State the blood parasite species.
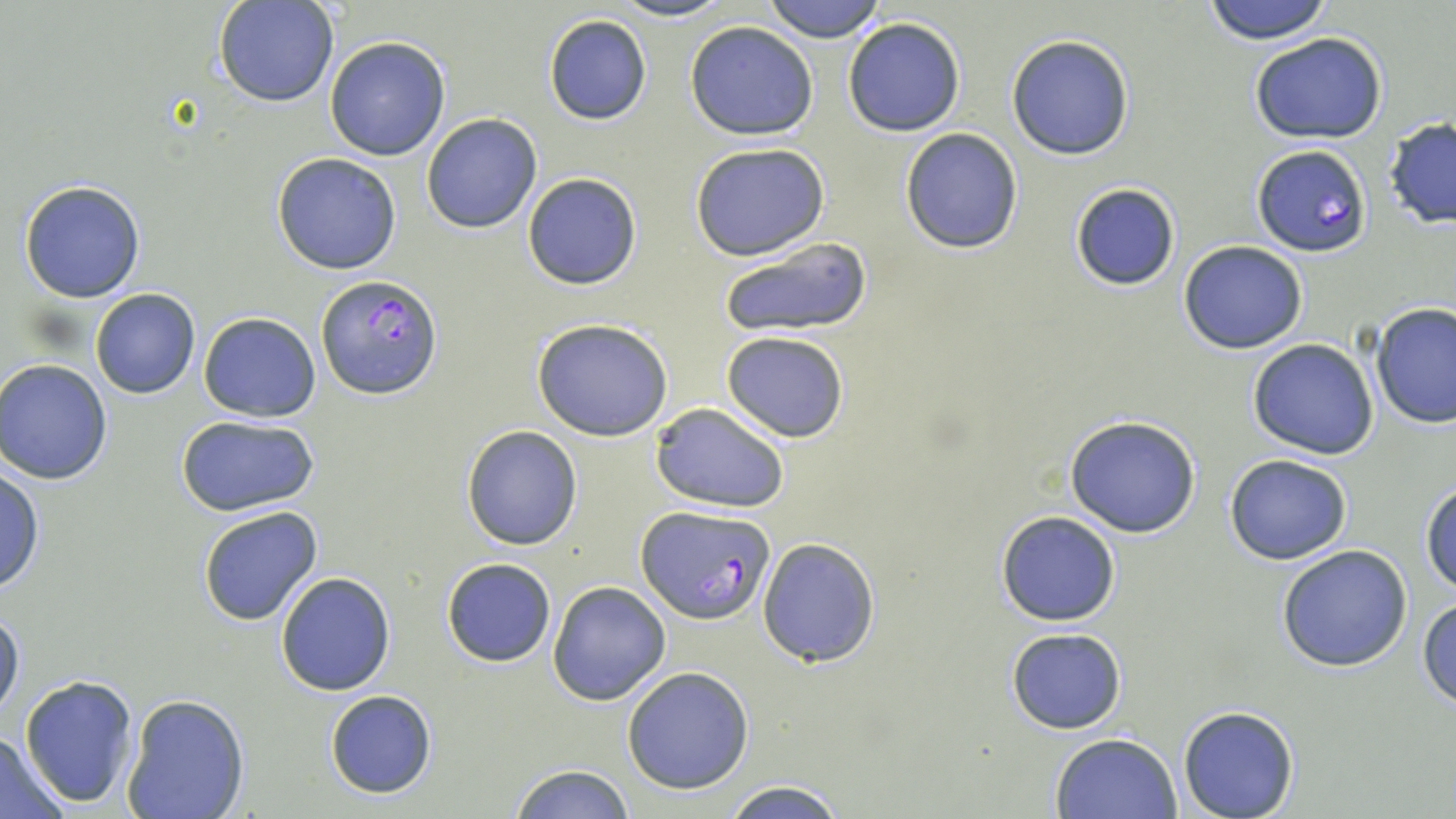

Plasmodium falciparum.

Approximate bounding boxes as named x1/y1/x2/y2 corners in pixels. Plasmodium falciparum-infected red blood cell locations: (x1=1250, y1=144, x2=1373, y2=257), (x1=316, y1=274, x2=442, y2=398), (x1=636, y1=505, x2=773, y2=623). Uninfected red blood cell locations: (x1=214, y1=0, x2=339, y2=106), (x1=610, y1=0, x2=736, y2=22), (x1=762, y1=0, x2=889, y2=42), (x1=1198, y1=1, x2=1337, y2=44), (x1=544, y1=15, x2=651, y2=125), (x1=843, y1=18, x2=965, y2=137), (x1=684, y1=22, x2=818, y2=140), (x1=1247, y1=31, x2=1389, y2=144), (x1=1005, y1=33, x2=1135, y2=160), (x1=324, y1=35, x2=450, y2=161), (x1=421, y1=113, x2=542, y2=234), (x1=1383, y1=118, x2=1456, y2=230), (x1=899, y1=128, x2=1024, y2=253), (x1=690, y1=142, x2=832, y2=261), (x1=272, y1=153, x2=402, y2=275), (x1=522, y1=172, x2=644, y2=290), (x1=19, y1=180, x2=146, y2=301), (x1=1068, y1=181, x2=1182, y2=293), (x1=715, y1=234, x2=873, y2=342), (x1=1178, y1=240, x2=1308, y2=353), (x1=90, y1=287, x2=200, y2=398), (x1=1371, y1=303, x2=1456, y2=429), (x1=199, y1=311, x2=321, y2=422), (x1=531, y1=318, x2=675, y2=441), (x1=721, y1=331, x2=850, y2=442), (x1=1247, y1=337, x2=1379, y2=460), (x1=2, y1=358, x2=117, y2=484), (x1=650, y1=401, x2=789, y2=514), (x1=176, y1=414, x2=319, y2=517), (x1=1063, y1=415, x2=1203, y2=538), (x1=461, y1=424, x2=582, y2=550), (x1=1224, y1=455, x2=1351, y2=565), (x1=0, y1=462, x2=43, y2=598), (x1=1421, y1=479, x2=1455, y2=593), (x1=197, y1=506, x2=324, y2=627), (x1=994, y1=511, x2=1121, y2=626), (x1=756, y1=536, x2=882, y2=667), (x1=1276, y1=544, x2=1414, y2=673), (x1=441, y1=557, x2=557, y2=667), (x1=276, y1=572, x2=395, y2=695), (x1=547, y1=581, x2=671, y2=704), (x1=1418, y1=597, x2=1456, y2=708), (x1=0, y1=605, x2=25, y2=723), (x1=1005, y1=628, x2=1128, y2=733), (x1=621, y1=666, x2=754, y2=794), (x1=19, y1=675, x2=140, y2=808), (x1=324, y1=689, x2=438, y2=799), (x1=121, y1=693, x2=249, y2=819), (x1=1178, y1=707, x2=1299, y2=819), (x1=1049, y1=731, x2=1182, y2=817), (x1=0, y1=733, x2=70, y2=817), (x1=509, y1=765, x2=634, y2=819), (x1=718, y1=778, x2=851, y2=819). One field of a larger specimen. Captured at 1000x magnification. May-Grünwald-Giemsa stain. Image is 1456×819 pixels. Thin blood film. Optical microscopy.